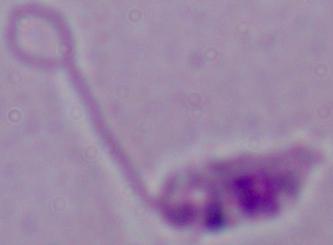 Micrograph. A Leishmania parasite is seen. 1000x magnification.